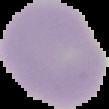

Summary:
  - Malaria status: uninfected
  - Preparation: thin blood film
  - Image size: 109×109 pixels
  - Image type: segmented cell region on a black background